Report the malaria status of this cell.
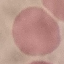

It is uninfected.

{
  "capture": "smartphone through the microscope eyepiece",
  "image_type": "automatically extracted cell patch, resized to 64 × 64 pixels",
  "preparation": "thin blood smear",
  "stain": "Giemsa"
}